Report the malaria status of this cell.
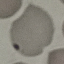

Uninfected.

preparation = thin blood film
image type = automatically extracted cell patch, resized to 64 × 64 pixels
capture = smartphone camera at the microscope eyepiece
stain = Giemsa